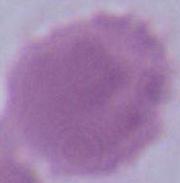

An erythrocyte is shown. Captured at 1000x magnification. Micrograph.